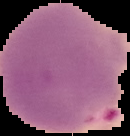
Summary:
  - Malaria status: parasitized
  - Image size: 130×136 pixels
  - Preparation: thin blood film
  - Image type: segmented cell region with the area outside set to black